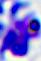
{
  "magnification": "400x",
  "modality": "micrograph",
  "identification": "leukocyte"
}